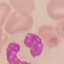
Result: negative for malaria parasites. Photographed with a smartphone camera at the microscope eyepiece. Automatically extracted cell patch, resized to 64 × 64 pixels. Giemsa stain. Thin smear of blood.